Outline each Plasmodium falciparum parasite and classify it by life-cycle stage.
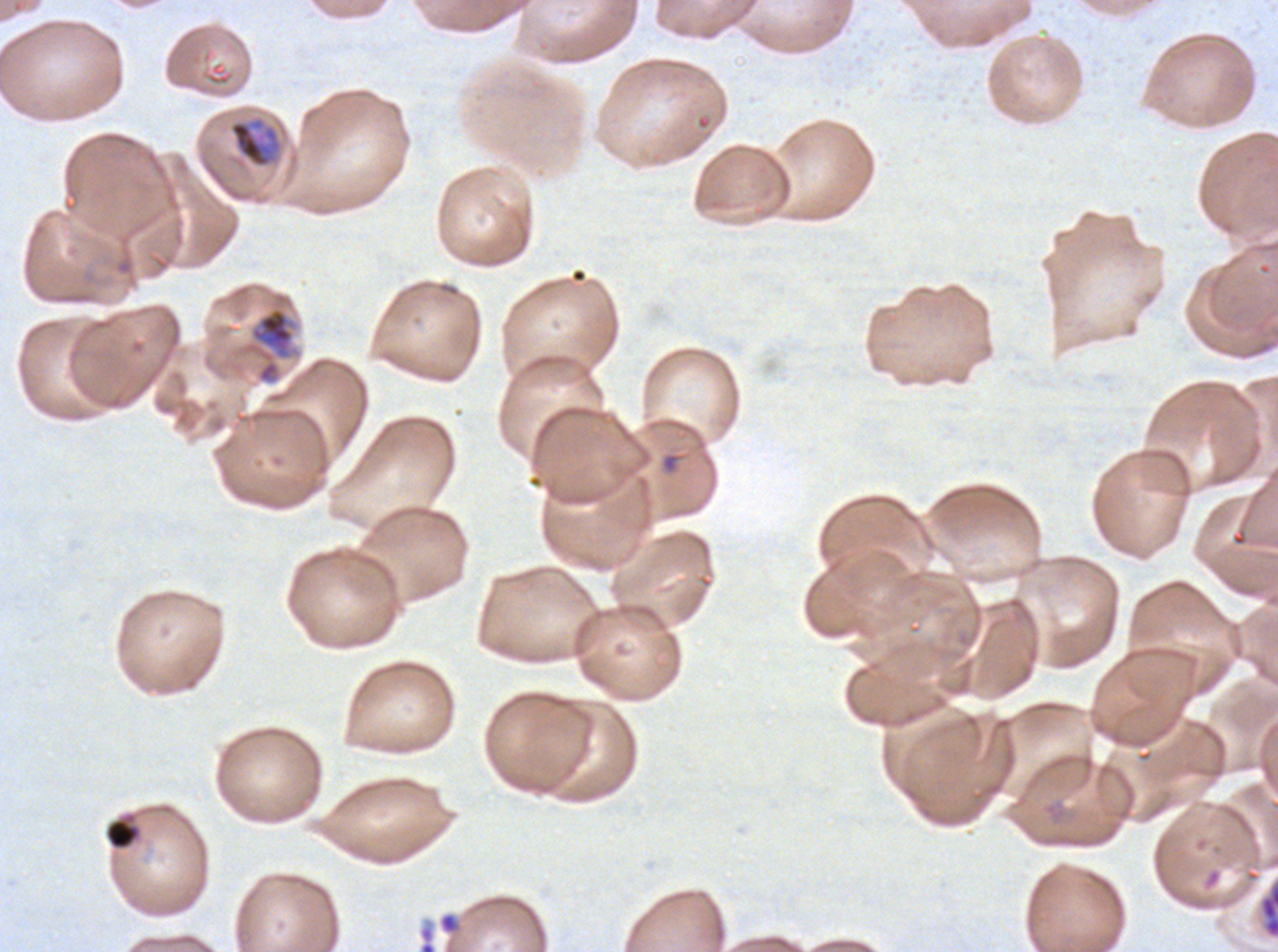
Approximate bounding boxes as {x1, y1, x2, y2} in pixels.
Mid trophozoites: {227, 116, 283, 169}, {241, 305, 300, 385}.
No rings, late-ring/early-trophozoite forms, late trophozoites, early schizonts, late schizonts, segmenters, or gametocytes observed.

Summary:
  - Debris locations: {105, 819, 139, 849}, {1259, 879, 1277, 939}, {438, 912, 460, 934}
  - Specimen: Plasmodium falciparum from a patient in The Gambia, cultured ex vivo for 24 to 48 hours
  - Image size: 1278×952 pixels
  - Field of view: sub-image separated from a larger composite
  - Stain: Giemsa
  - Preparation: thin blood smear